Comment on the morphology of the red blood cells.
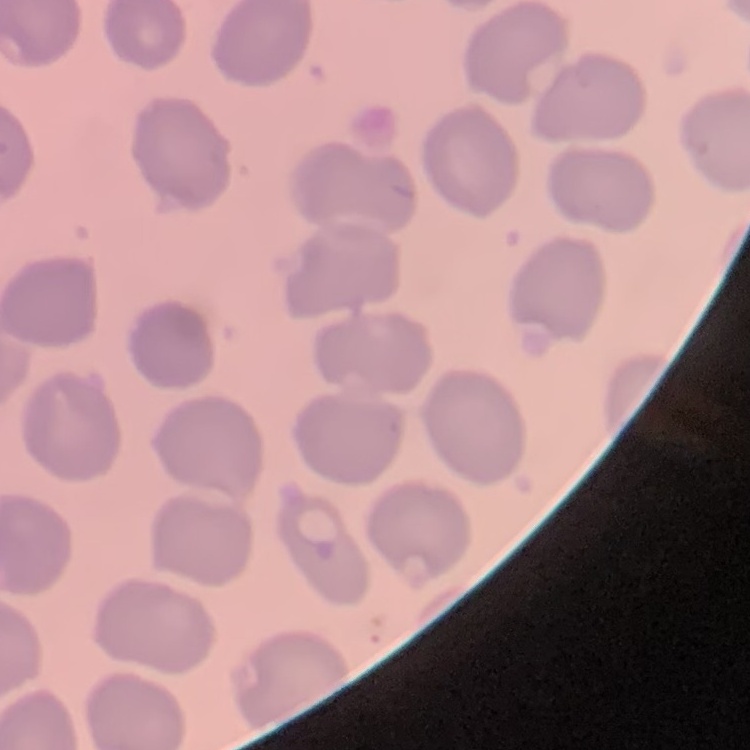

They show no rouleaux formation.

{
  "image_type": "square crop of a larger photomicrograph",
  "preparation": "thin peripheral smear",
  "stain": "Field's or Giemsa"
}